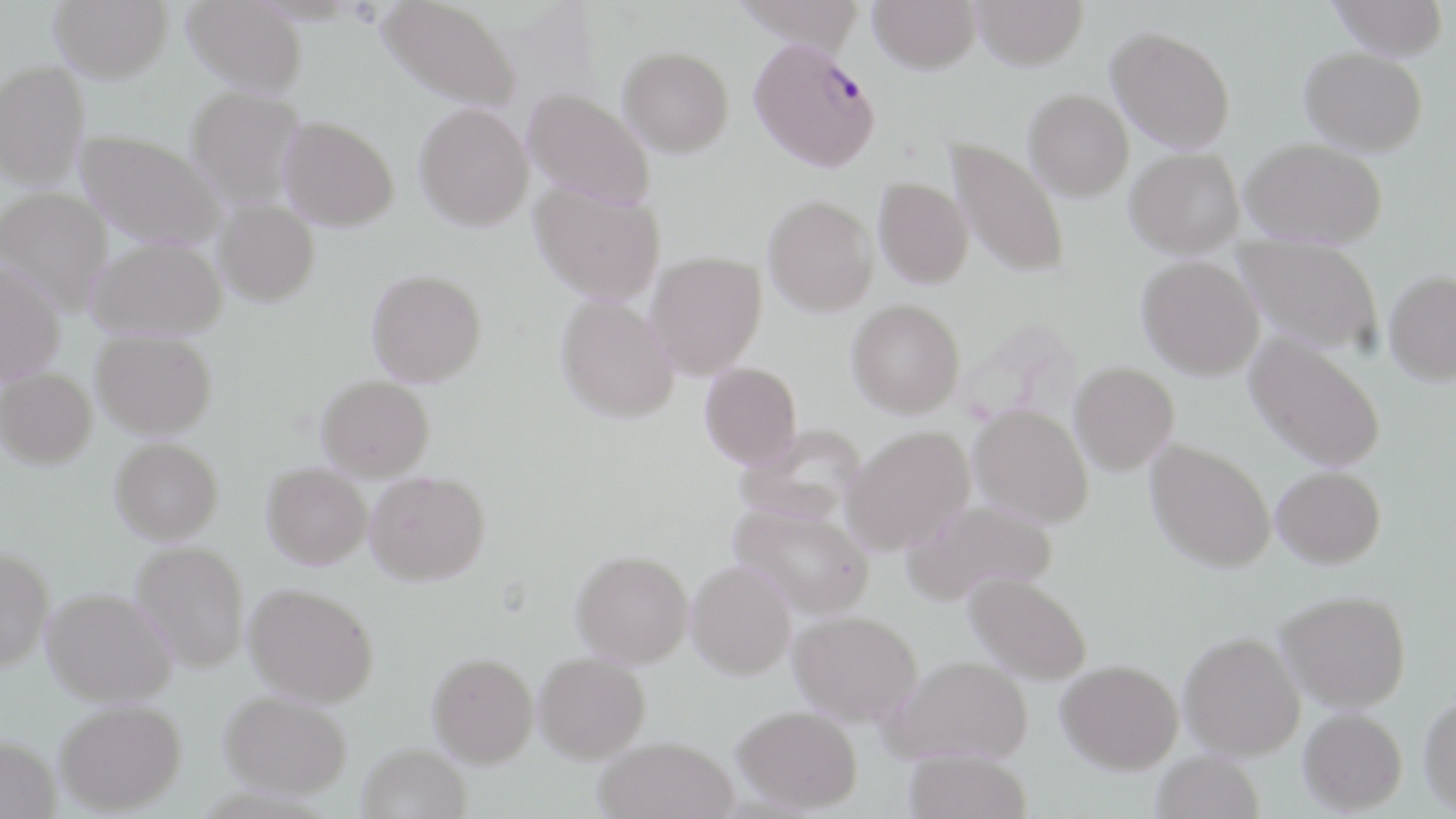

Summary:
  - Coordinate format: approximate bounding boxes as (x1, y1, x2, y2) in pixels
  - Uninfected red blood cell locations: (49, 0, 173, 82), (183, 0, 307, 96), (378, 0, 521, 112), (733, 0, 869, 54), (868, 0, 981, 73), (972, 0, 1088, 70), (1327, 0, 1449, 59), (1107, 26, 1235, 153), (618, 46, 734, 156), (1300, 47, 1427, 154), (0, 60, 90, 189), (186, 86, 306, 208), (523, 88, 655, 209), (1024, 89, 1133, 201), (414, 102, 534, 231), (279, 116, 399, 231), (76, 130, 228, 249), (948, 138, 1070, 280), (1241, 139, 1388, 247), (1125, 147, 1244, 257), (873, 177, 974, 288), (530, 180, 665, 304), (0, 186, 113, 316), (763, 195, 878, 316), (213, 200, 320, 306), (1233, 234, 1384, 356), (86, 237, 226, 339), (646, 251, 767, 379), (1136, 255, 1264, 380), (0, 259, 65, 384), (367, 269, 487, 386), (1383, 270, 1456, 385), (556, 294, 680, 423), (846, 299, 965, 418), (92, 330, 217, 438), (1245, 333, 1386, 473), (700, 362, 802, 467), (1069, 362, 1179, 475), (0, 368, 97, 469), (317, 375, 434, 480), (969, 404, 1093, 527), (736, 424, 866, 524), (842, 425, 975, 554), (110, 437, 223, 543), (1145, 439, 1276, 573), (262, 462, 372, 569), (1272, 466, 1385, 568), (365, 470, 491, 585), (902, 498, 1058, 606), (732, 504, 874, 618), (131, 540, 251, 672), (0, 547, 54, 671), (571, 549, 694, 667), (687, 560, 796, 679), (965, 571, 1093, 684), (244, 582, 379, 707), (43, 587, 176, 706), (1276, 590, 1412, 712), (789, 610, 922, 724), (1179, 630, 1306, 761), (533, 651, 651, 762), (428, 652, 538, 766), (882, 655, 1033, 766), (1056, 659, 1183, 773), (220, 690, 354, 798), (1418, 692, 1456, 815), (55, 699, 186, 814), (733, 705, 863, 812), (1298, 707, 1407, 814), (0, 735, 60, 819), (594, 737, 738, 819), (357, 743, 471, 819), (903, 748, 1032, 819), (1151, 750, 1264, 819)
  - Plasmodium falciparum-infected red blood cell locations: (748, 38, 880, 171)
  - Slide-level diagnosis: Plasmodium falciparum
  - Preparation: thin blood film
  - Field of view: single
  - Image size: 1456×819 pixels
  - Magnification: 1000x
  - Stain: May-Grünwald-Giemsa
  - Modality: optical microscopy